Report the malaria status of this cell.
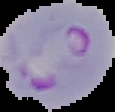
It is parasitized.

{
  "image_type": "segmented cell region on a black background",
  "image_size": "115×112 pixels",
  "preparation": "thin blood film"
}